Outline each Plasmodium falciparum-infected red blood cell.
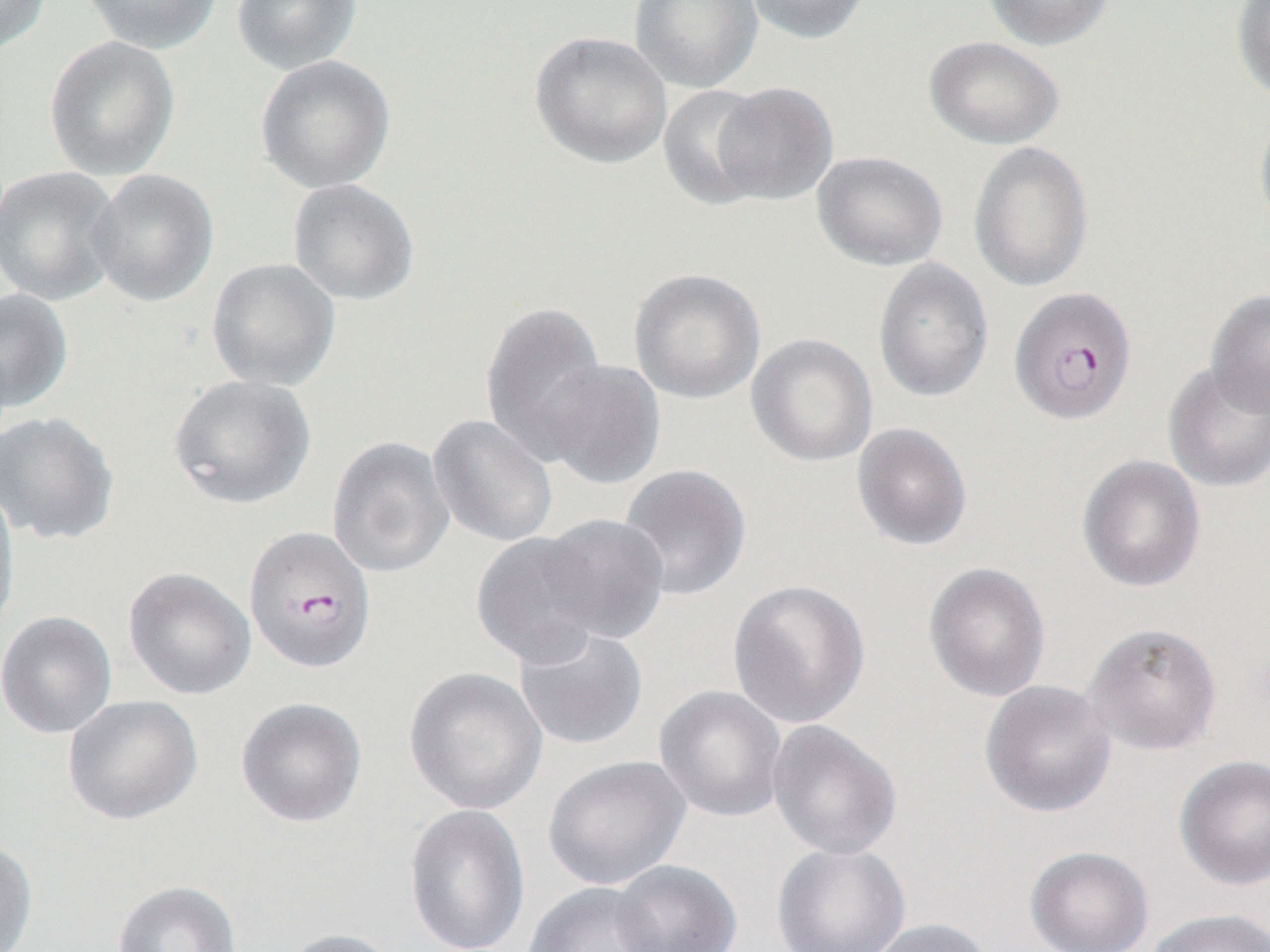
Approximate bounding boxes as (x1,y1)-(x2,y2) corner pairs in pixels.
Plasmodium falciparum-infected red blood cells: (1009,286)-(1137,425), (244,525)-(377,673).

Summary:
  - Uninfected red blood cell locations: (0,0)-(50,55), (81,0)-(223,53), (231,0)-(363,74), (629,0)-(763,93), (742,0)-(872,45), (980,0)-(1117,51), (1231,1)-(1270,103), (530,31)-(673,168), (44,35)-(181,181), (924,35)-(1065,150), (255,55)-(396,194), (711,81)-(839,205), (656,84)-(775,210), (1253,107)-(1270,243), (968,140)-(1094,293), (812,150)-(948,271), (0,166)-(122,305), (87,168)-(219,307), (288,178)-(420,305), (207,258)-(341,392), (873,258)-(994,403), (629,268)-(766,405), (1205,288)-(1270,418), (0,289)-(74,412), (480,299)-(609,461), (747,333)-(879,468), (538,359)-(666,489), (1163,362)-(1270,493), (167,374)-(316,510), (0,410)-(120,546), (428,414)-(558,548), (852,423)-(972,550), (327,436)-(454,578), (1077,454)-(1206,593), (618,464)-(751,601), (0,483)-(21,644), (537,513)-(670,644), (472,531)-(610,668), (924,562)-(1051,703), (123,566)-(256,700), (729,579)-(871,729), (0,611)-(117,739), (1082,621)-(1222,755), (513,625)-(649,751), (404,666)-(547,815), (980,680)-(1117,818), (654,685)-(788,823), (63,694)-(203,825), (236,697)-(367,827), (767,720)-(902,861), (543,754)-(691,890), (1174,755)-(1270,890), (403,804)-(530,951), (0,838)-(38,952), (771,842)-(911,952), (1025,846)-(1154,952), (612,860)-(743,952), (112,880)-(242,952), (523,882)-(670,952), (1143,907)-(1269,952), (863,918)-(995,952), (274,927)-(406,952)
  - Slide-level diagnosis: Plasmodium falciparum
  - Field of view: one of a larger specimen
  - Preparation: thin blood smear
  - Image size: 1270×952 pixels
  - Modality: light microscopy
  - Magnification: 1000x